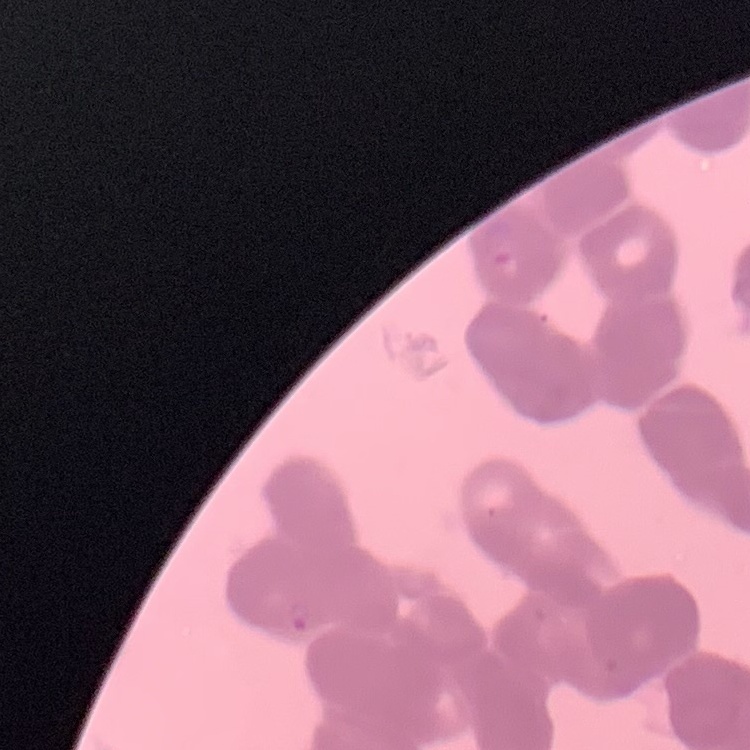

{
  "red_blood_cell_morphology": "rouleaux formation",
  "stain": "Field's or Giemsa",
  "image_type": "square crop of a larger photomicrograph",
  "preparation": "thin blood film"
}